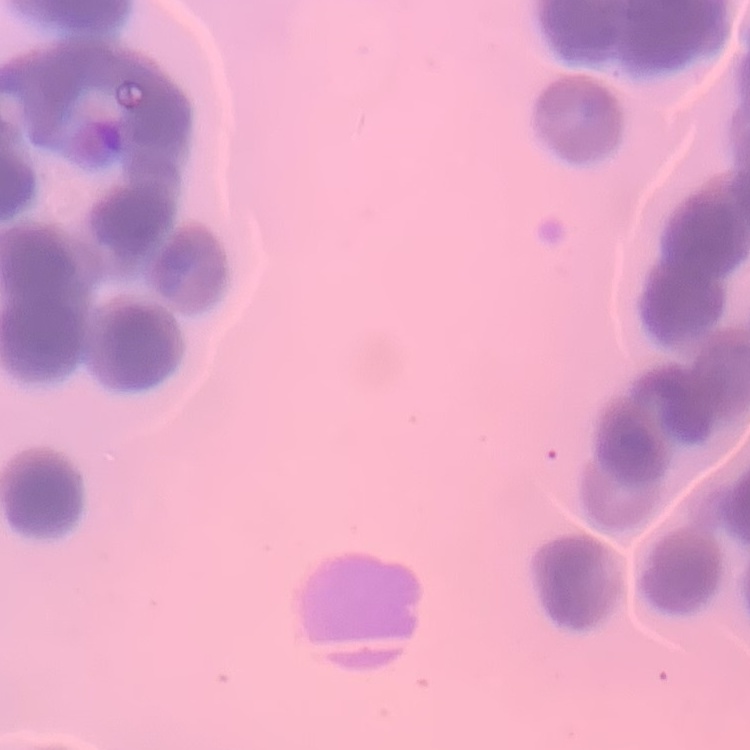
The erythrocytes exhibit rouleaux formation. Field's or Giemsa stain. Thin peripheral smear. One tile cut from a larger photomicrograph.